Report the malaria status of this cell.
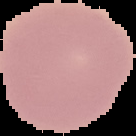
It is uninfected.

Summary:
  - Image size: 136×136 pixels
  - Image type: segmented cell region on a black background
  - Preparation: thin blood film